Name the cell type shown.
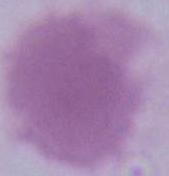
An erythrocyte.

modality = micrograph
magnification = 1000x